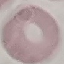
Malaria status: uninfected. Photographed with a smartphone camera at the microscope eyepiece. Automatically extracted cell patch, resized to 64 × 64 pixels. Thin blood film. Giemsa-stained preparation.